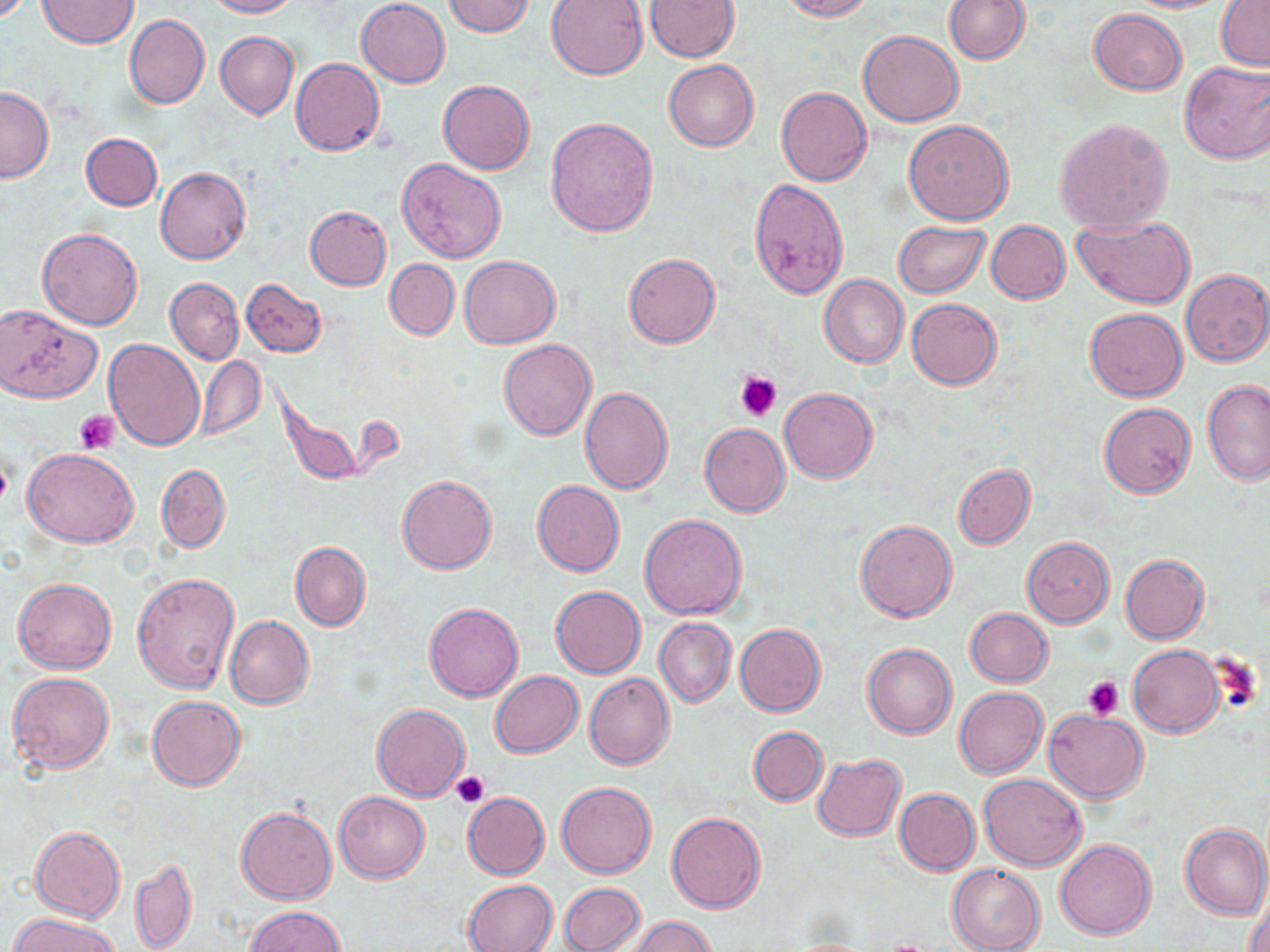
slide-level diagnosis = no evidence of blood parasites
platelet locations = approximate bounding boxes as [x1, y1, x2, y2] in pixels: [736, 371, 782, 422], [75, 411, 120, 453], [1207, 653, 1266, 715], [1084, 675, 1124, 718], [452, 771, 490, 809]
preparation = thin blood smear
modality = optical microscopy
stain = May-Grünwald-Giemsa
uninfected red blood cell locations = approximate bounding boxes as [x1, y1, x2, y2] in pixels: [205, 0, 298, 18], [355, 0, 450, 87], [546, 0, 648, 79], [645, 0, 738, 61], [779, 0, 873, 21], [944, 0, 1028, 64], [1119, 0, 1232, 13], [1216, 0, 1270, 70], [37, 1, 137, 49], [443, 1, 536, 37], [1089, 9, 1187, 95], [124, 14, 209, 109], [857, 30, 963, 126], [216, 32, 297, 119], [290, 58, 385, 156], [664, 59, 758, 152], [1179, 60, 1270, 164], [438, 80, 535, 174], [0, 85, 53, 185], [776, 86, 871, 186], [545, 116, 658, 237], [1054, 117, 1174, 234], [903, 120, 1014, 223], [81, 133, 162, 210], [396, 158, 507, 263], [156, 168, 249, 264], [749, 179, 849, 299], [305, 206, 391, 290], [1073, 214, 1195, 309], [893, 220, 990, 297], [986, 220, 1069, 303], [37, 228, 142, 330], [623, 253, 718, 348], [459, 255, 559, 348], [385, 258, 459, 339], [1181, 269, 1270, 367], [819, 275, 908, 369], [165, 277, 243, 365], [241, 278, 327, 357], [907, 299, 1002, 389], [0, 304, 103, 402], [1085, 306, 1188, 401], [104, 337, 205, 449], [499, 339, 596, 439], [197, 356, 265, 439], [1201, 378, 1270, 484], [580, 386, 673, 493], [780, 388, 877, 483], [1099, 401, 1197, 498], [699, 423, 790, 517], [23, 447, 138, 548], [953, 463, 1035, 549], [156, 464, 230, 553], [397, 475, 497, 574], [532, 481, 624, 576], [640, 513, 746, 619], [855, 519, 957, 622], [1022, 537, 1114, 628], [290, 540, 370, 631], [1120, 554, 1209, 644], [132, 571, 239, 693], [13, 578, 116, 673], [551, 585, 646, 678], [424, 602, 523, 700], [965, 608, 1053, 686], [225, 616, 314, 709], [655, 618, 735, 707], [734, 623, 826, 717], [862, 643, 957, 738], [1128, 645, 1224, 737], [490, 671, 583, 757], [7, 672, 114, 775], [584, 672, 675, 769], [954, 687, 1047, 777], [147, 696, 245, 790], [952, 700, 1141, 791], [372, 704, 468, 800], [1044, 709, 1150, 803], [748, 726, 828, 806], [813, 754, 906, 840], [978, 773, 1088, 870], [557, 780, 656, 878], [894, 787, 980, 875], [334, 791, 428, 883], [462, 793, 548, 879], [236, 807, 335, 904], [666, 811, 767, 912], [1180, 821, 1270, 918], [29, 825, 125, 922], [1055, 839, 1156, 940], [129, 858, 197, 952], [947, 864, 1046, 952], [462, 879, 557, 952], [558, 881, 645, 952], [1245, 886, 1270, 952], [245, 905, 344, 952], [7, 914, 122, 952], [623, 916, 720, 952]
field of view = one of a larger specimen
image size = 1270×952 pixels
magnification = 1000x